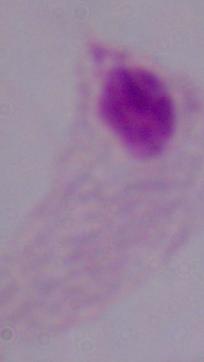

Summary:
  - Magnification: 1000x
  - Identification: trichomonad
  - Modality: micrograph